Evaluate for Plasmodium parasites.
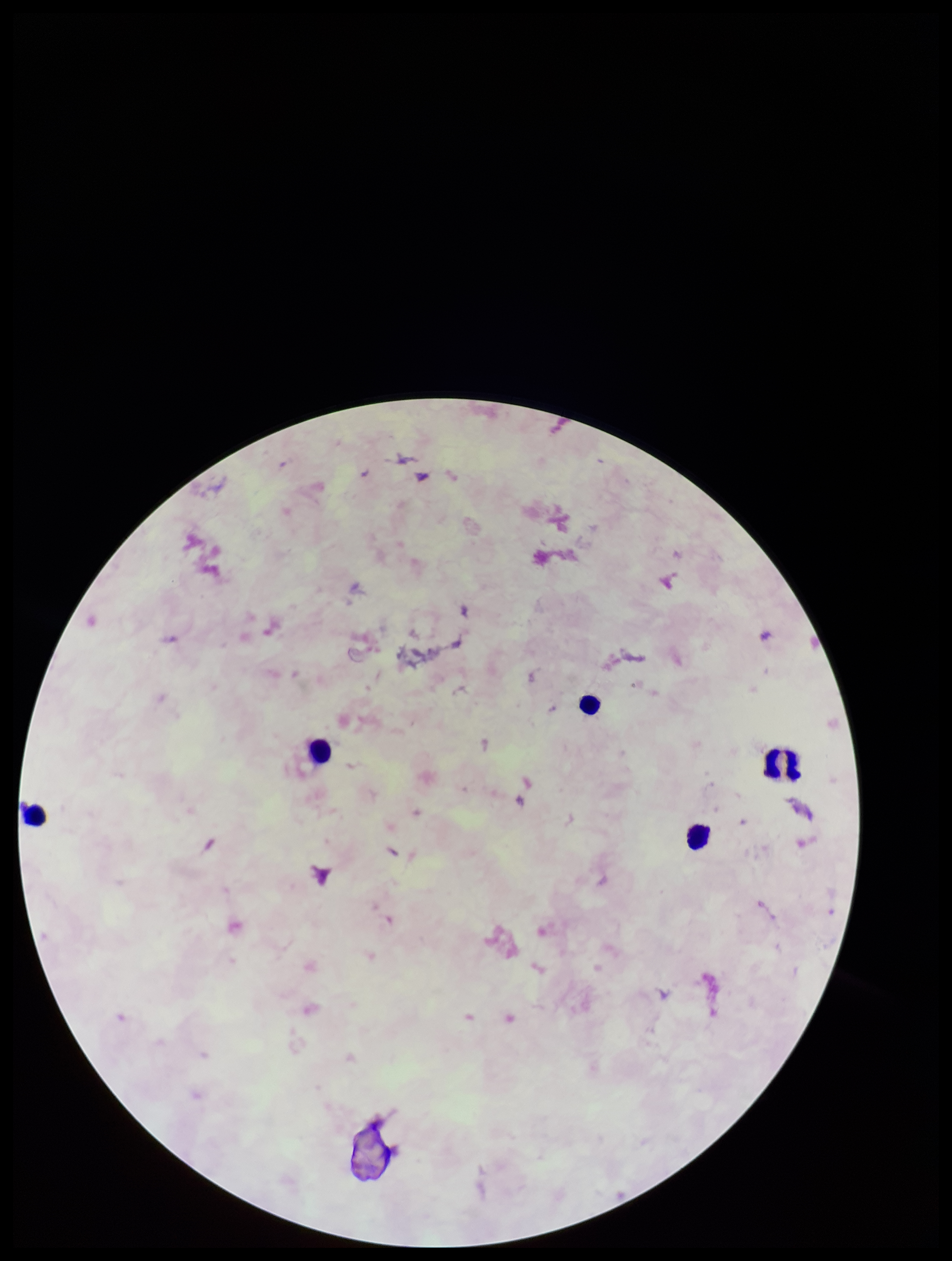

None detected.

Parasite count: 0. Preparation: thick. Stained with Giemsa. One field from this slide. Image is 952×1261 pixels. Leukocyte count: 5. Photographed through the microscope eyepiece with a smartphone camera. Patient malaria status: negative.